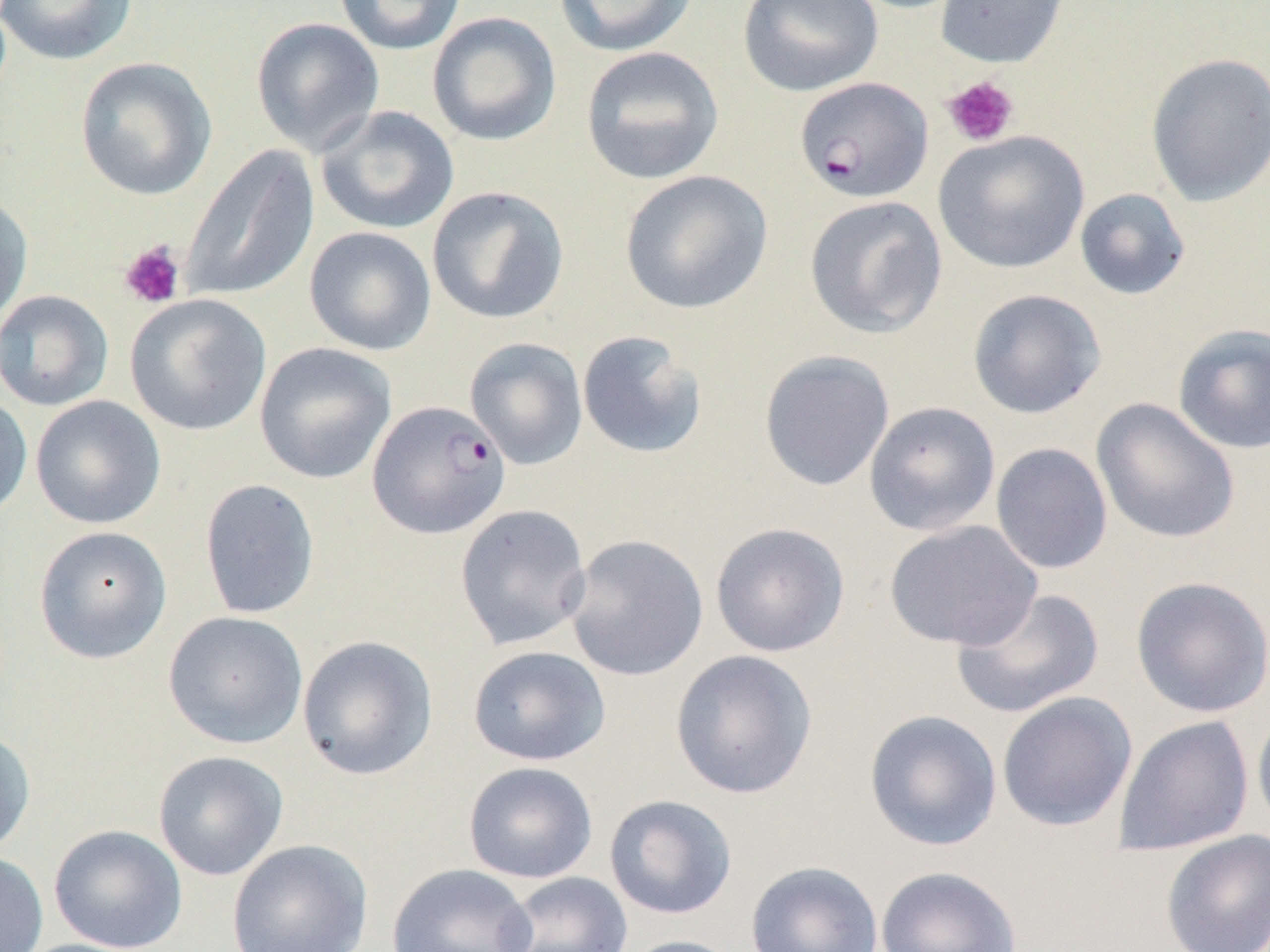
Summary:
  - Coordinate format: approximate bounding boxes as [x1, y1, x2, y2] in pixels
  - Uninfected red blood cell locations: [0, 0, 137, 66], [333, 0, 467, 55], [737, 0, 883, 97], [934, 0, 1071, 69], [553, 1, 700, 57], [427, 12, 562, 147], [250, 16, 385, 156], [579, 46, 724, 185], [1145, 52, 1270, 207], [74, 56, 217, 202], [315, 105, 459, 235], [933, 129, 1089, 274], [180, 145, 319, 303], [619, 170, 773, 315], [426, 186, 570, 324], [1074, 187, 1191, 301], [0, 189, 33, 332], [804, 195, 948, 339], [304, 226, 437, 356], [967, 288, 1106, 419], [0, 290, 114, 411], [125, 294, 272, 436], [1172, 324, 1270, 454], [576, 330, 709, 460], [465, 336, 589, 470], [254, 342, 397, 485], [759, 350, 895, 491], [0, 391, 33, 522], [30, 395, 166, 529], [1092, 399, 1240, 545], [863, 401, 1001, 536], [990, 442, 1113, 574], [199, 478, 321, 620], [454, 503, 592, 651], [884, 519, 1043, 651], [710, 521, 851, 658], [33, 525, 172, 664], [564, 533, 709, 681], [1130, 576, 1270, 718], [949, 587, 1105, 719], [162, 610, 309, 749], [297, 635, 439, 781], [467, 645, 611, 766], [669, 649, 818, 800], [996, 691, 1138, 833], [1252, 706, 1270, 841], [864, 709, 1003, 851], [1113, 715, 1255, 856], [0, 728, 36, 857], [153, 750, 288, 880], [463, 761, 598, 883], [604, 794, 738, 920], [49, 824, 188, 952], [1159, 829, 1270, 951], [226, 839, 373, 952], [0, 851, 49, 952], [745, 860, 884, 952], [387, 863, 535, 951], [875, 865, 1022, 952], [497, 871, 633, 952], [617, 935, 746, 952]
  - Platelet locations: [942, 75, 1019, 147], [118, 240, 186, 309]
  - Plasmodium falciparum-infected red blood cell locations: [794, 76, 934, 203], [367, 400, 512, 540]
  - Slide-level diagnosis: Plasmodium falciparum
  - Preparation: thin blood film
  - Modality: light microscopy
  - Field of view: one of a larger specimen
  - Image size: 1270×952 pixels
  - Magnification: 1000x